Give the position of every Plasmodium parasite visible.
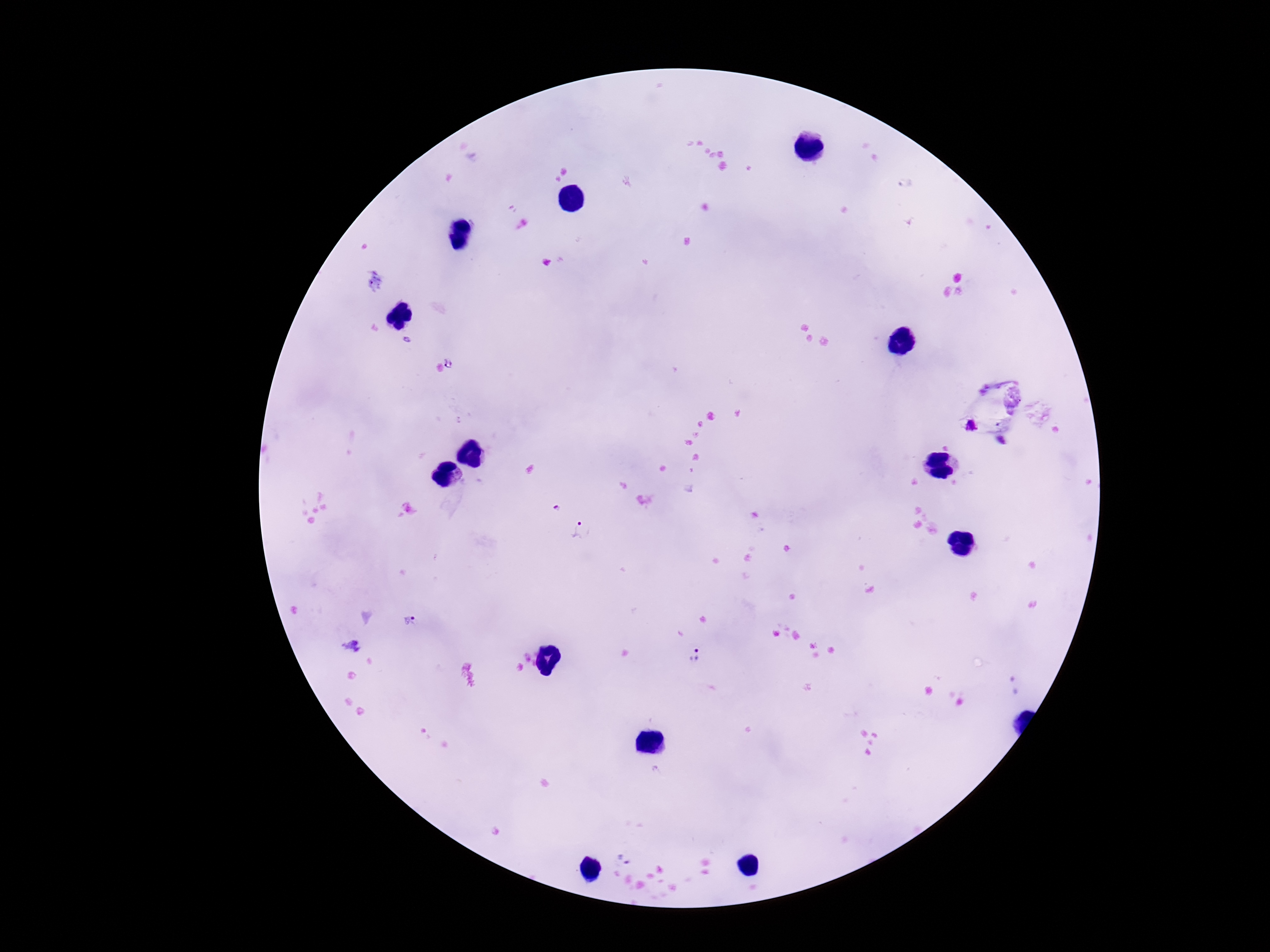

Approximate centers as {x, y} in pixels.
Plasmodium parasites: {407, 341}, {454, 361}, {970, 426}, {555, 507}, {579, 530}, {408, 623}, {351, 643}, {697, 661}, {1015, 684}, {625, 858}.

Thick blood film. Giemsa stain. Image is 1270×952 pixels. Photographed through the microscope eyepiece with a smartphone camera. 100x magnification. One field from this slide. Patient malaria status: positive.